Report the malaria status of this cell.
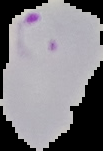

Parasitized.

image_type: segmented cell region on a black background
image_size: 103×151 pixels
preparation: thin blood smear